Comment on the morphology of the red blood cells.
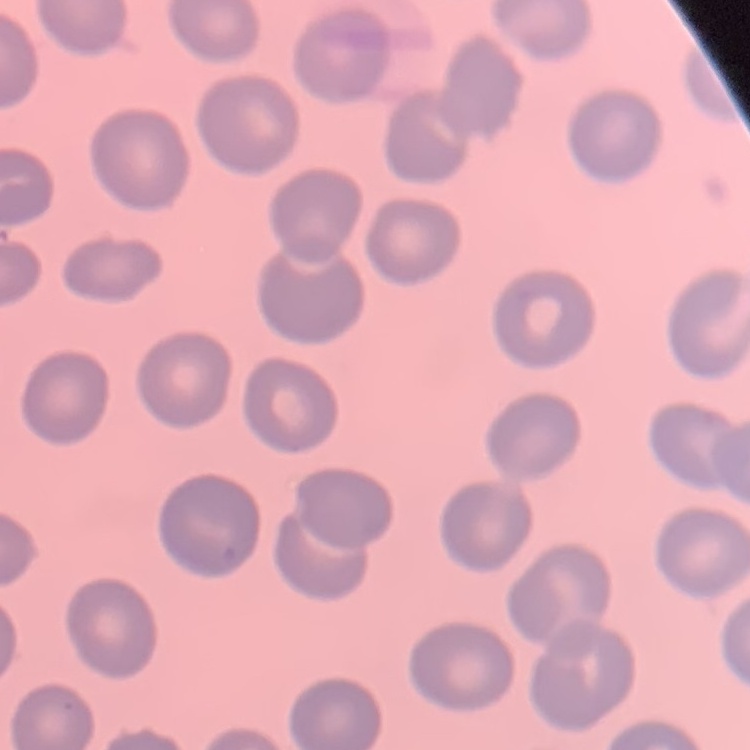
No rouleaux formation.

Square crop of a larger photomicrograph. Field's or Giemsa stain. Thin blood film.